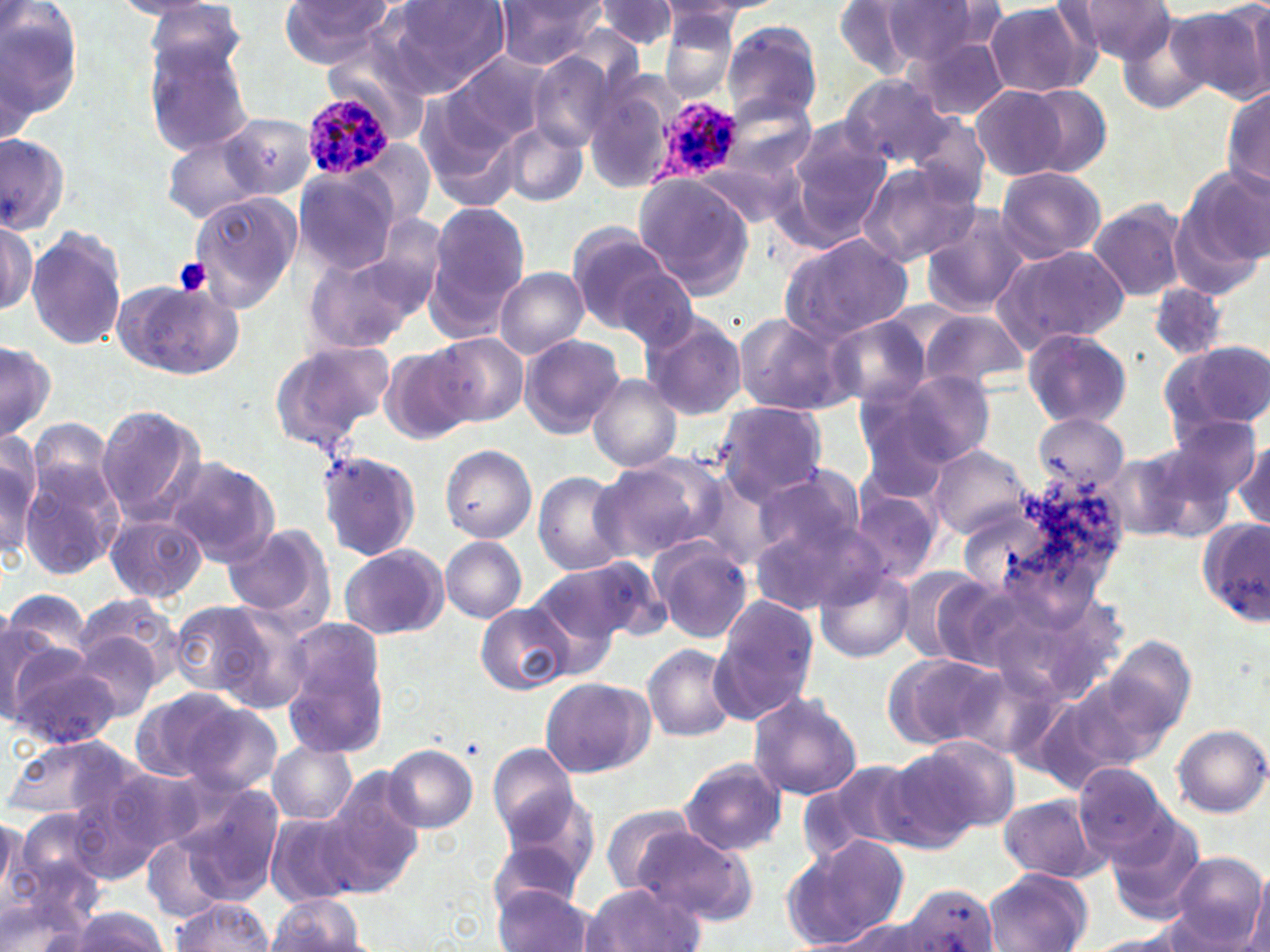
slide_level_diagnosis: Plasmodium ovale
platelet_locations: 'approximate bounding boxes as (x1, y1, x2, y2) in pixels: (174, 257, 212, 296)'
plasmodium_ovale_infected_red_blood_cell_locations: 'approximate bounding boxes as (x1, y1, x2, y2) in pixels: (304, 96, 394, 177), (646, 96, 741, 194)'
image_size: 1270×952 pixels
magnification: 1000x
uninfected_red_blood_cell_locations: 'approximate bounding boxes as (x1, y1, x2, y2) in pixels: (107, 0, 233, 21), (277, 0, 398, 69), (382, 0, 511, 96), (492, 0, 608, 69), (660, 0, 781, 22), (1063, 0, 1178, 65), (593, 1, 682, 52), (832, 1, 928, 80), (982, 1, 1097, 97), (140, 2, 253, 74), (878, 2, 995, 68), (1172, 3, 1269, 101), (0, 4, 86, 136), (659, 11, 740, 100), (1113, 11, 1215, 115), (722, 21, 822, 123), (909, 37, 1010, 121), (319, 38, 431, 137), (142, 40, 256, 154), (527, 51, 619, 152), (438, 52, 552, 158), (843, 75, 954, 167), (581, 79, 676, 194), (1221, 80, 1269, 203), (970, 85, 1072, 182), (1021, 85, 1112, 178), (724, 98, 815, 181), (900, 108, 991, 209), (221, 111, 319, 198), (497, 121, 586, 207), (786, 121, 892, 236), (160, 130, 267, 224), (0, 134, 71, 235), (353, 138, 433, 228), (854, 161, 980, 267), (1181, 165, 1269, 275), (995, 166, 1106, 263), (293, 168, 399, 275), (634, 176, 755, 297), (189, 190, 302, 309), (1088, 198, 1188, 303), (426, 202, 529, 329), (917, 207, 1029, 317), (1, 216, 37, 316), (566, 224, 677, 332), (25, 227, 126, 351), (778, 233, 914, 346), (991, 244, 1129, 353), (301, 245, 432, 359), (495, 267, 588, 358), (614, 268, 702, 353), (116, 279, 241, 380), (1148, 284, 1226, 364), (918, 310, 1027, 391), (639, 312, 747, 421), (732, 312, 855, 418), (824, 316, 932, 409), (1021, 328, 1133, 428), (519, 333, 626, 439), (433, 334, 529, 427), (0, 339, 55, 442), (267, 339, 395, 456), (1158, 339, 1270, 437), (379, 343, 475, 443), (870, 369, 997, 471), (585, 374, 683, 471), (711, 401, 829, 505), (853, 404, 964, 504), (95, 405, 205, 524), (1029, 412, 1129, 495), (1155, 418, 1262, 516), (0, 434, 41, 559), (1230, 441, 1269, 531), (438, 444, 537, 543), (928, 445, 1030, 538), (317, 451, 421, 562), (1105, 452, 1194, 542), (594, 455, 723, 562), (18, 456, 126, 578), (166, 456, 281, 565), (749, 467, 869, 569), (532, 471, 633, 577), (850, 488, 943, 584), (750, 511, 882, 615), (105, 513, 206, 604), (1197, 518, 1267, 626), (222, 523, 333, 626), (440, 536, 528, 624), (651, 539, 753, 643), (339, 544, 447, 640), (558, 558, 668, 642), (815, 563, 916, 661), (527, 564, 638, 663), (904, 568, 1014, 672), (2, 594, 84, 701), (73, 595, 187, 691), (711, 595, 821, 722), (167, 599, 275, 701), (212, 602, 316, 711), (476, 605, 573, 694), (281, 619, 391, 758), (3, 621, 53, 726), (71, 631, 165, 723), (1102, 635, 1196, 743), (2, 644, 119, 750), (643, 645, 737, 742), (882, 652, 1003, 749), (954, 662, 1065, 758), (540, 677, 652, 778), (129, 690, 244, 784), (746, 692, 862, 801), (174, 697, 285, 797), (1170, 722, 1269, 817), (3, 733, 136, 823), (908, 737, 1019, 833), (267, 741, 356, 825), (383, 745, 478, 833), (488, 747, 580, 844), (878, 750, 983, 851), (678, 757, 788, 856), (1077, 760, 1169, 860), (97, 762, 208, 864), (320, 779, 423, 894), (180, 785, 284, 900), (497, 788, 600, 889), (997, 793, 1108, 885), (596, 806, 701, 892), (1103, 809, 1207, 925), (265, 811, 361, 906), (0, 813, 31, 914), (631, 826, 756, 925), (142, 830, 236, 920), (785, 833, 913, 948), (486, 842, 585, 918), (1167, 852, 1266, 950), (983, 869, 1092, 951), (1249, 872, 1270, 952), (581, 883, 704, 952), (899, 883, 1000, 952), (492, 884, 595, 952), (267, 894, 366, 951), (0, 896, 98, 950), (170, 899, 273, 950), (60, 909, 172, 952), (838, 917, 935, 952), (1083, 933, 1193, 951)'
stain: May-Grünwald-Giemsa
field_of_view: single
preparation: thin blood film
modality: light microscopy